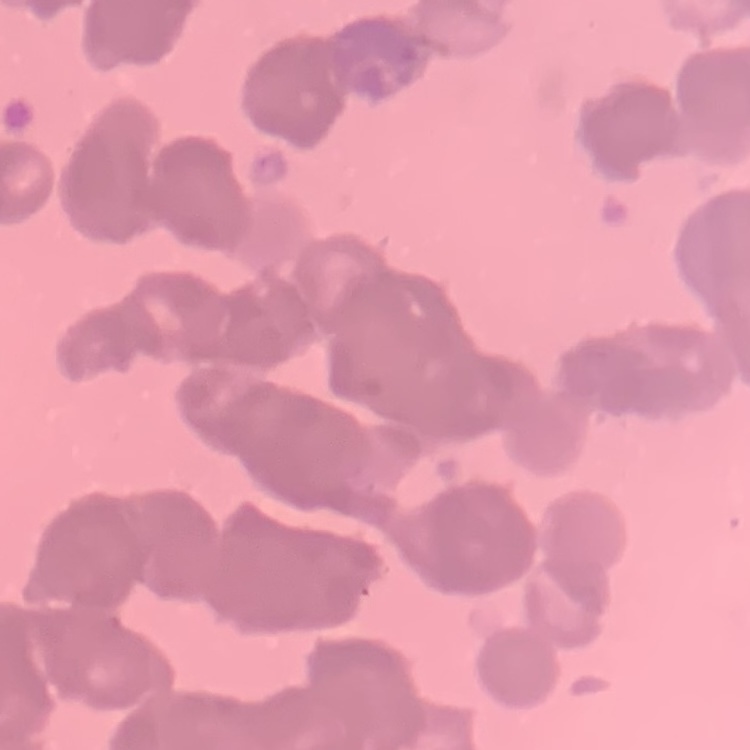
The erythrocytes show rouleaux formation. Thin peripheral smear. Field's or Giemsa stain. One tile cut from a larger photomicrograph.